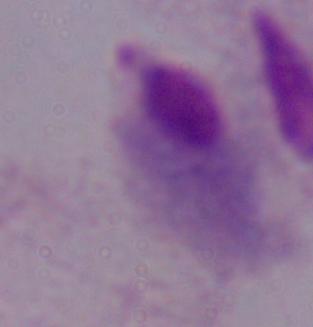

A trichomonad is seen. Captured at 1000x magnification. Photomicrograph.